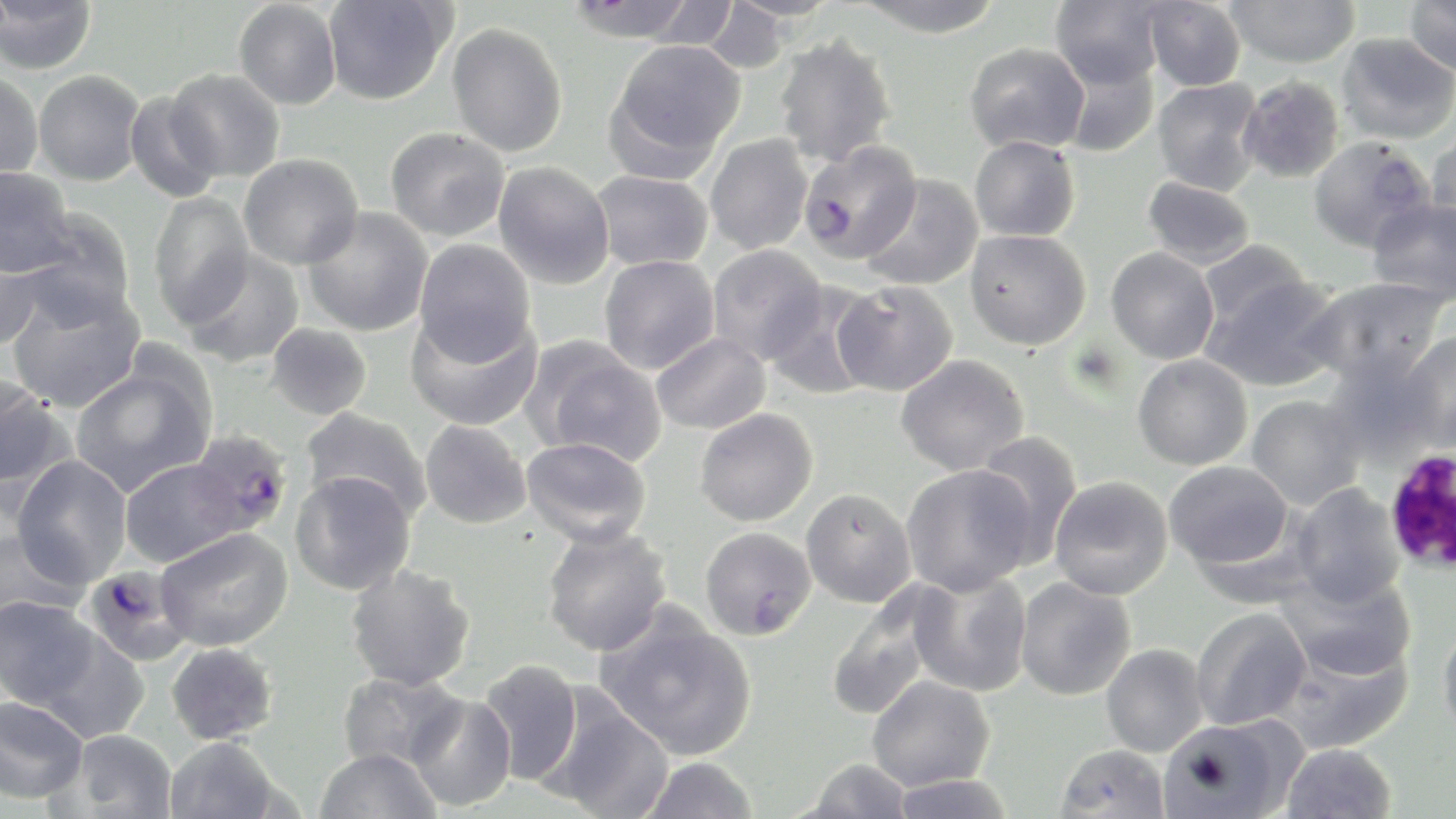

Approximate bounding boxes as named x1/y1/x2/y2 corners in pixels. Plasmodium falciparum-infected red blood cell locations: (x1=799, y1=139, x2=923, y2=265), (x1=185, y1=430, x2=293, y2=541), (x1=82, y1=565, x2=194, y2=667). White blood cell locations: (x1=1383, y1=446, x2=1456, y2=576). Uninfected red blood cell locations: (x1=322, y1=0, x2=453, y2=105), (x1=564, y1=0, x2=700, y2=42), (x1=635, y1=0, x2=742, y2=49), (x1=854, y1=0, x2=1007, y2=37), (x1=1050, y1=0, x2=1164, y2=89), (x1=1142, y1=0, x2=1246, y2=91), (x1=1225, y1=0, x2=1360, y2=68), (x1=1404, y1=0, x2=1456, y2=76), (x1=0, y1=1, x2=98, y2=75), (x1=233, y1=1, x2=342, y2=110), (x1=698, y1=2, x2=794, y2=73), (x1=446, y1=22, x2=568, y2=157), (x1=1336, y1=32, x2=1456, y2=145), (x1=773, y1=33, x2=898, y2=167), (x1=607, y1=39, x2=746, y2=171), (x1=964, y1=42, x2=1089, y2=155), (x1=1058, y1=55, x2=1159, y2=158), (x1=165, y1=68, x2=285, y2=182), (x1=32, y1=70, x2=146, y2=186), (x1=0, y1=71, x2=44, y2=183), (x1=1237, y1=75, x2=1346, y2=183), (x1=1152, y1=78, x2=1265, y2=195), (x1=124, y1=91, x2=223, y2=203), (x1=385, y1=127, x2=509, y2=241), (x1=1427, y1=129, x2=1456, y2=238), (x1=705, y1=134, x2=814, y2=254), (x1=969, y1=136, x2=1080, y2=242), (x1=1308, y1=136, x2=1435, y2=253), (x1=239, y1=153, x2=364, y2=269), (x1=493, y1=162, x2=615, y2=289), (x1=0, y1=166, x2=75, y2=277), (x1=592, y1=170, x2=713, y2=271), (x1=861, y1=174, x2=984, y2=291), (x1=1142, y1=176, x2=1256, y2=270), (x1=148, y1=192, x2=255, y2=327), (x1=1366, y1=196, x2=1456, y2=305), (x1=302, y1=206, x2=434, y2=336), (x1=20, y1=208, x2=136, y2=324), (x1=964, y1=229, x2=1092, y2=350), (x1=0, y1=238, x2=47, y2=351), (x1=413, y1=239, x2=537, y2=364), (x1=1198, y1=239, x2=1312, y2=332), (x1=706, y1=244, x2=828, y2=364), (x1=1105, y1=247, x2=1220, y2=364), (x1=181, y1=249, x2=304, y2=369), (x1=599, y1=254, x2=720, y2=374), (x1=1204, y1=275, x2=1344, y2=391), (x1=1303, y1=277, x2=1448, y2=385), (x1=6, y1=280, x2=146, y2=413), (x1=832, y1=281, x2=958, y2=396), (x1=764, y1=283, x2=880, y2=400), (x1=406, y1=308, x2=543, y2=431), (x1=265, y1=323, x2=373, y2=421), (x1=1394, y1=331, x2=1456, y2=450), (x1=651, y1=332, x2=770, y2=434), (x1=526, y1=339, x2=667, y2=466), (x1=1321, y1=350, x2=1441, y2=465), (x1=895, y1=354, x2=1029, y2=475), (x1=1132, y1=354, x2=1254, y2=470), (x1=70, y1=361, x2=215, y2=497), (x1=1, y1=376, x2=69, y2=494), (x1=1246, y1=394, x2=1366, y2=510), (x1=301, y1=407, x2=432, y2=521), (x1=694, y1=408, x2=818, y2=526), (x1=420, y1=420, x2=532, y2=529), (x1=971, y1=430, x2=1084, y2=563), (x1=520, y1=436, x2=652, y2=547), (x1=10, y1=455, x2=132, y2=587), (x1=119, y1=457, x2=254, y2=567), (x1=1165, y1=460, x2=1295, y2=569), (x1=901, y1=464, x2=1036, y2=596), (x1=290, y1=471, x2=417, y2=596), (x1=1049, y1=476, x2=1173, y2=600), (x1=1290, y1=484, x2=1407, y2=606), (x1=801, y1=488, x2=916, y2=608), (x1=0, y1=525, x2=88, y2=627), (x1=541, y1=525, x2=672, y2=657), (x1=155, y1=526, x2=293, y2=651), (x1=699, y1=527, x2=816, y2=640), (x1=346, y1=564, x2=477, y2=691), (x1=905, y1=569, x2=1034, y2=698), (x1=1280, y1=569, x2=1416, y2=682), (x1=1014, y1=577, x2=1136, y2=701), (x1=824, y1=595, x2=940, y2=721), (x1=0, y1=596, x2=98, y2=708), (x1=1191, y1=606, x2=1311, y2=730), (x1=596, y1=607, x2=758, y2=761), (x1=1438, y1=619, x2=1456, y2=740), (x1=35, y1=630, x2=150, y2=745), (x1=1277, y1=632, x2=1413, y2=754), (x1=165, y1=642, x2=279, y2=745), (x1=1101, y1=643, x2=1208, y2=757), (x1=476, y1=659, x2=583, y2=786), (x1=336, y1=671, x2=466, y2=772), (x1=867, y1=675, x2=995, y2=791), (x1=535, y1=689, x2=674, y2=819), (x1=405, y1=692, x2=516, y2=812), (x1=0, y1=695, x2=90, y2=804), (x1=1156, y1=717, x2=1298, y2=819), (x1=61, y1=728, x2=178, y2=818), (x1=164, y1=737, x2=282, y2=819), (x1=1055, y1=743, x2=1170, y2=818), (x1=1281, y1=743, x2=1397, y2=819), (x1=313, y1=748, x2=441, y2=819), (x1=639, y1=756, x2=759, y2=818), (x1=802, y1=758, x2=914, y2=818), (x1=886, y1=773, x2=1019, y2=818). Slide-level diagnosis: Plasmodium falciparum. 1000x magnification. May-Grünwald-Giemsa-stained preparation. Thin blood smear. Image is 1456×819 pixels. Light microscopy. Single field of view.